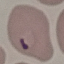
Summary:
  - Result: malaria parasites identified
  - Stain: Giemsa
  - Image type: cell patch, automatically extracted from a larger field of view and resized to 64 × 64 pixels
  - Capture: smartphone camera at the microscope eyepiece
  - Preparation: thin blood film